Assess the morphology of the erythrocytes.
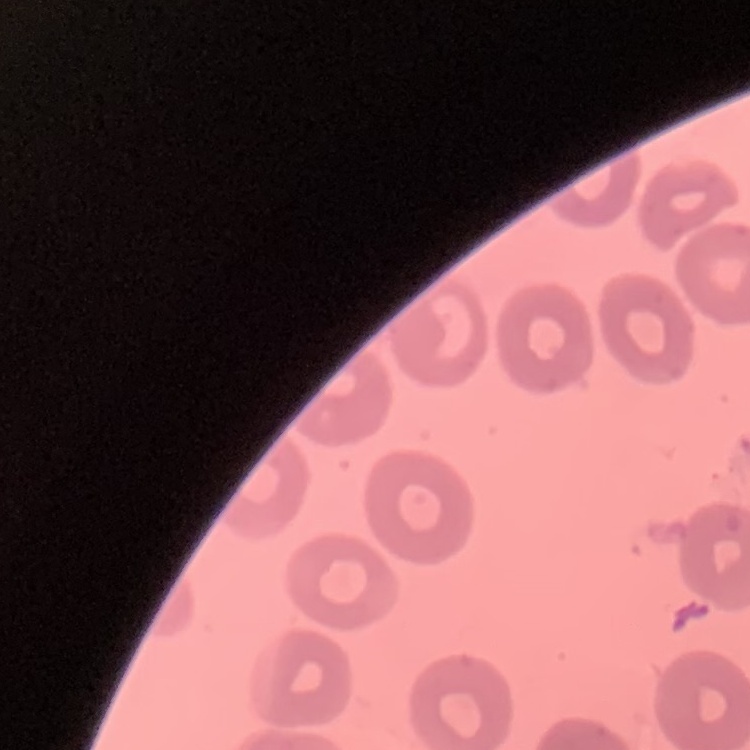
They show no rouleaux formation.

Summary:
  - Image type: square crop of a larger photomicrograph
  - Preparation: thin blood film
  - Stain: Field's or Giemsa